Evaluate for Plasmodium parasites.
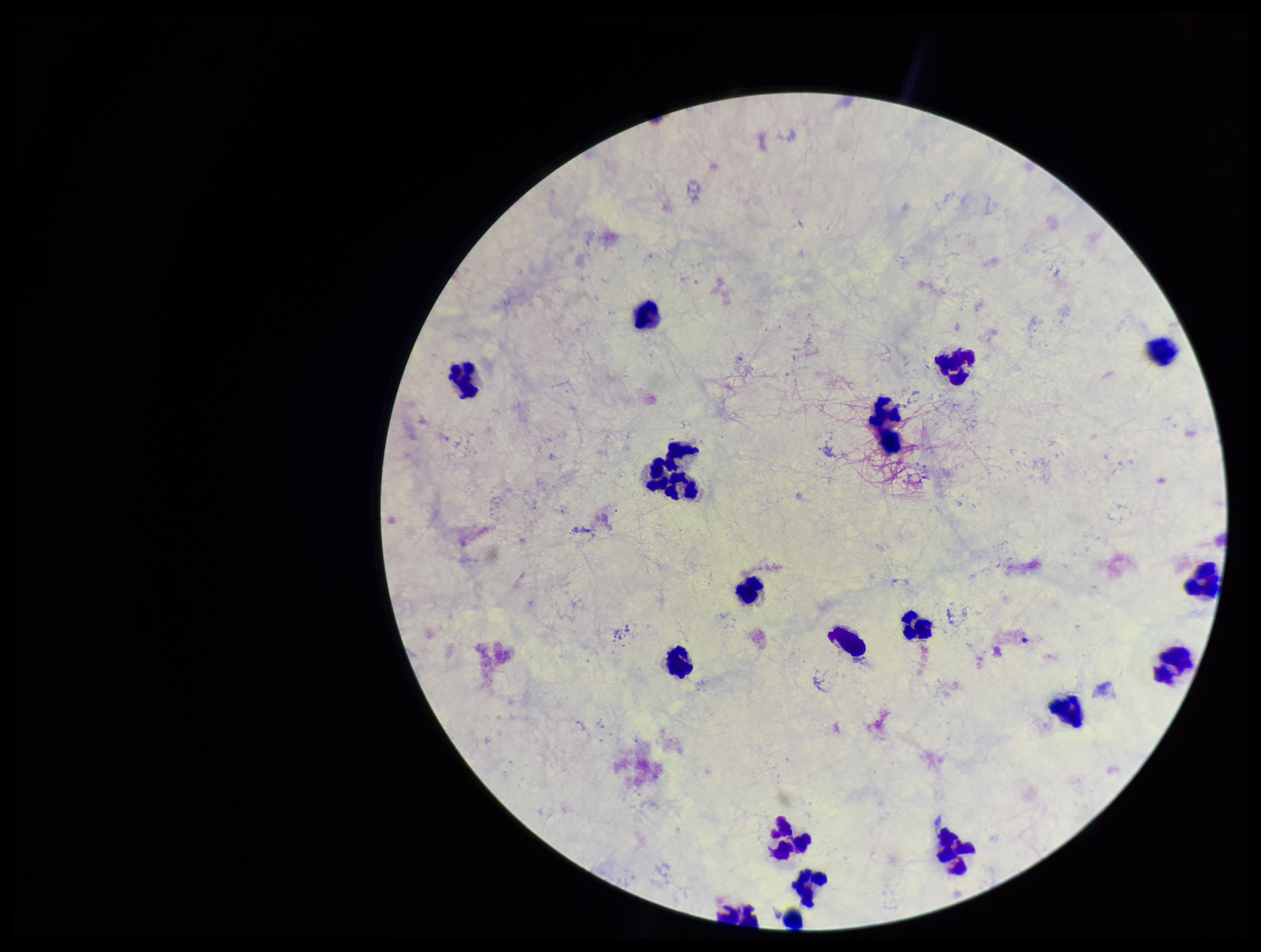
None detected.

Summary:
  - Stain: Giemsa
  - Capture: smartphone photograph through the microscope eyepiece
  - Patient malaria status: negative
  - Leukocyte count: 18
  - Parasite count: 0
  - Field of view: single
  - Preparation: thick
  - Image size: 1261×952 pixels